Classify this cell by malaria status.
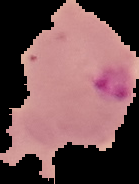
It is parasitized.

Segmented cell region on a black background. Image is 139×184 pixels. From a thin blood film.